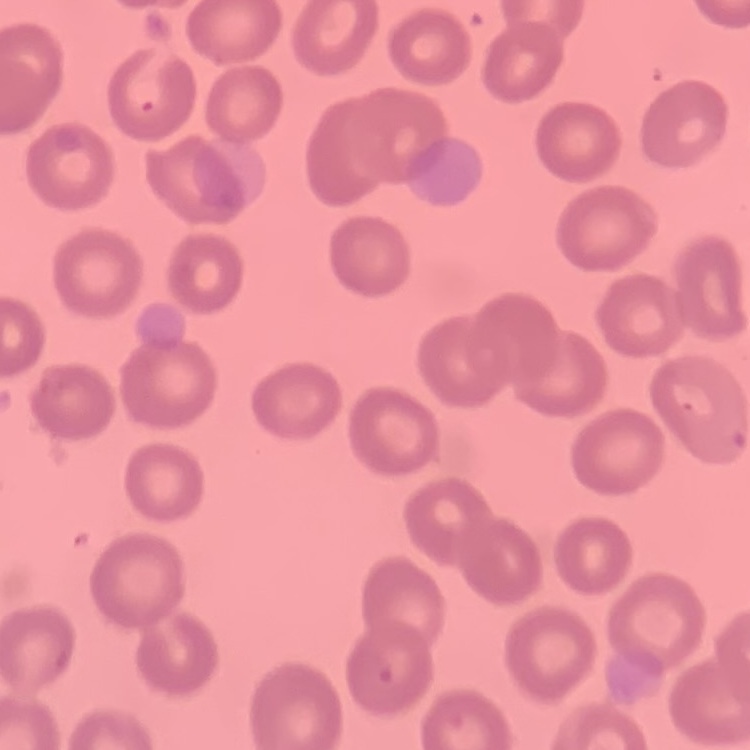 The red blood cells show no rouleaux formation. One tile cut from a larger photomicrograph. Thin peripheral smear. Field's or Giemsa stain.